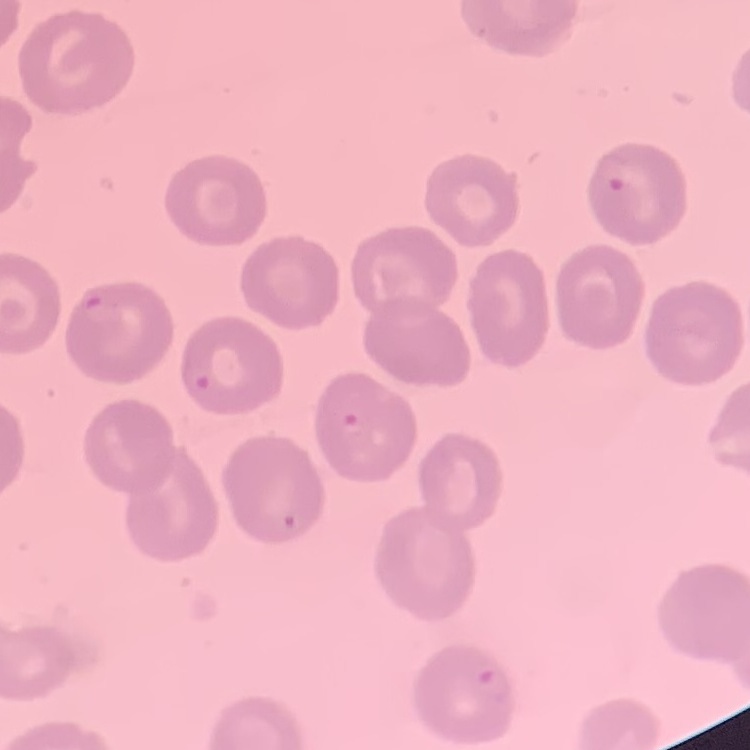
erythrocyte_morphology: no rouleaux formation
image_type: square crop of a larger photomicrograph
preparation: thin peripheral smear
stain: Field's or Giemsa